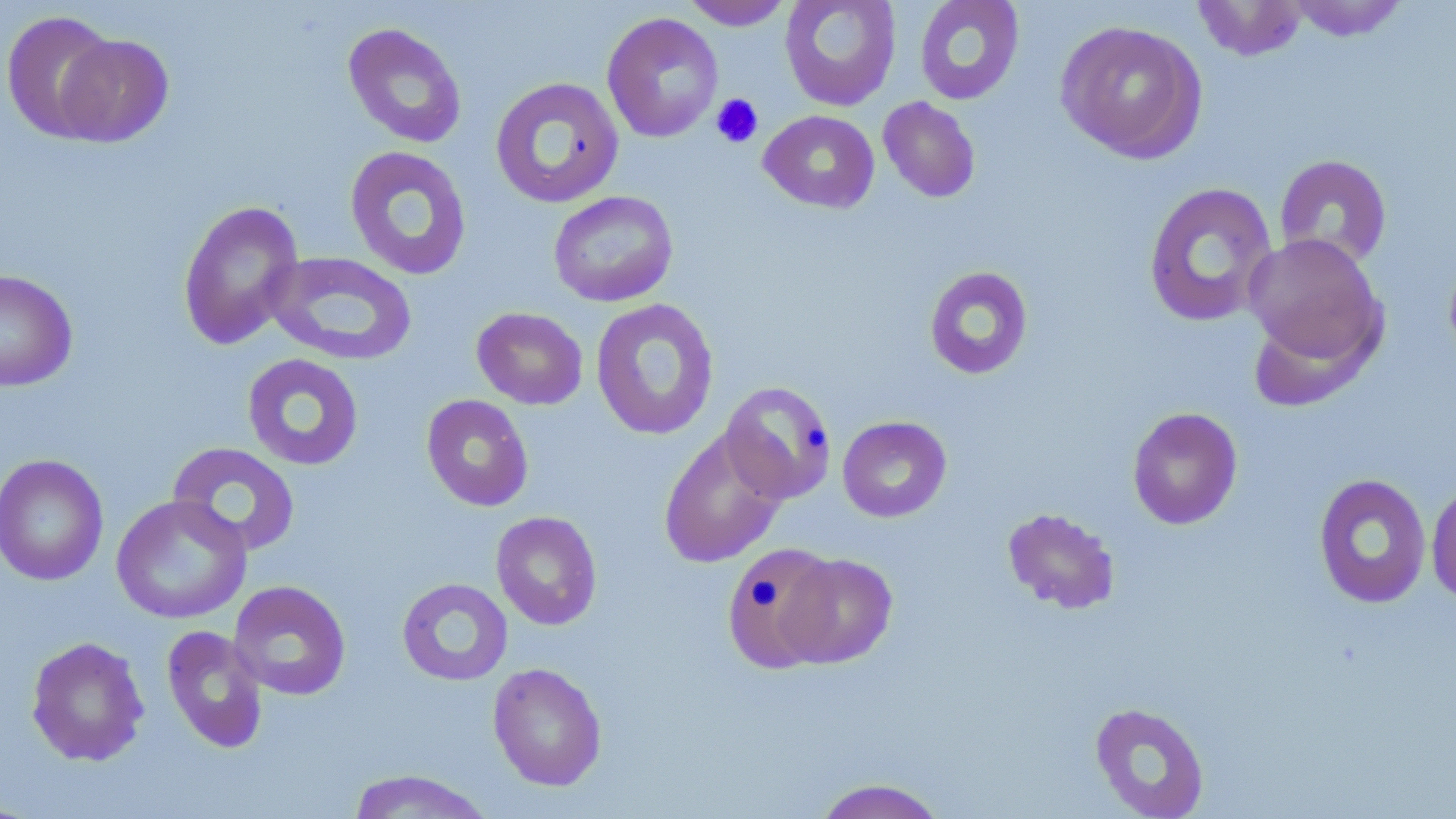
Approximate bounding boxes as (x1,y1)-(x2,y2) corner pairs in pixels. Uninfected red blood cell locations: (780,0)-(901,111), (913,0)-(1025,106), (1192,0)-(1308,61), (1287,0)-(1408,41), (681,1)-(794,30), (0,10)-(120,142), (601,12)-(723,143), (1055,20)-(1207,164), (342,22)-(467,149), (54,33)-(174,147), (490,76)-(624,208), (877,97)-(981,203), (758,110)-(880,214), (344,145)-(473,280), (1273,154)-(1393,270), (1143,182)-(1278,328), (548,190)-(678,307), (177,200)-(304,350), (1243,234)-(1386,370), (1443,246)-(1456,370), (264,251)-(417,366), (924,265)-(1034,380), (0,269)-(78,392), (590,298)-(720,441), (471,307)-(588,410), (242,353)-(365,471), (720,380)-(837,504), (421,394)-(534,512), (1127,406)-(1243,530), (837,416)-(952,523), (658,429)-(787,569), (167,442)-(301,557), (0,453)-(109,586), (1313,473)-(1432,610), (1426,479)-(1456,605), (110,494)-(252,624), (1001,507)-(1121,615), (490,511)-(603,630), (721,542)-(843,673), (777,553)-(898,668), (396,577)-(513,686), (228,580)-(351,701), (161,625)-(269,754), (25,636)-(150,767), (488,662)-(607,791), (1089,701)-(1210,818), (345,769)-(497,818), (811,777)-(949,819). Platelet locations: (710,93)-(764,149). Slide-level diagnosis: negative for blood parasites. May-Grünwald-Giemsa-stained preparation. Single field of view. Thin blood smear. Optical microscopy. Captured at 1000x magnification. Image is 1456×819 pixels.